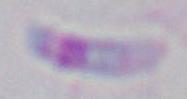 Toxoplasma gondii is shown. Micrograph. Captured at 1000x magnification.